Report the malaria status of this cell.
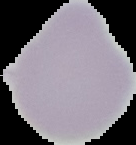
It is uninfected.

preparation: thin blood film
image_type: cell region segmented out of the field of view; surrounding area masked to black
image_size: 136×145 pixels